Identify the preparation type.
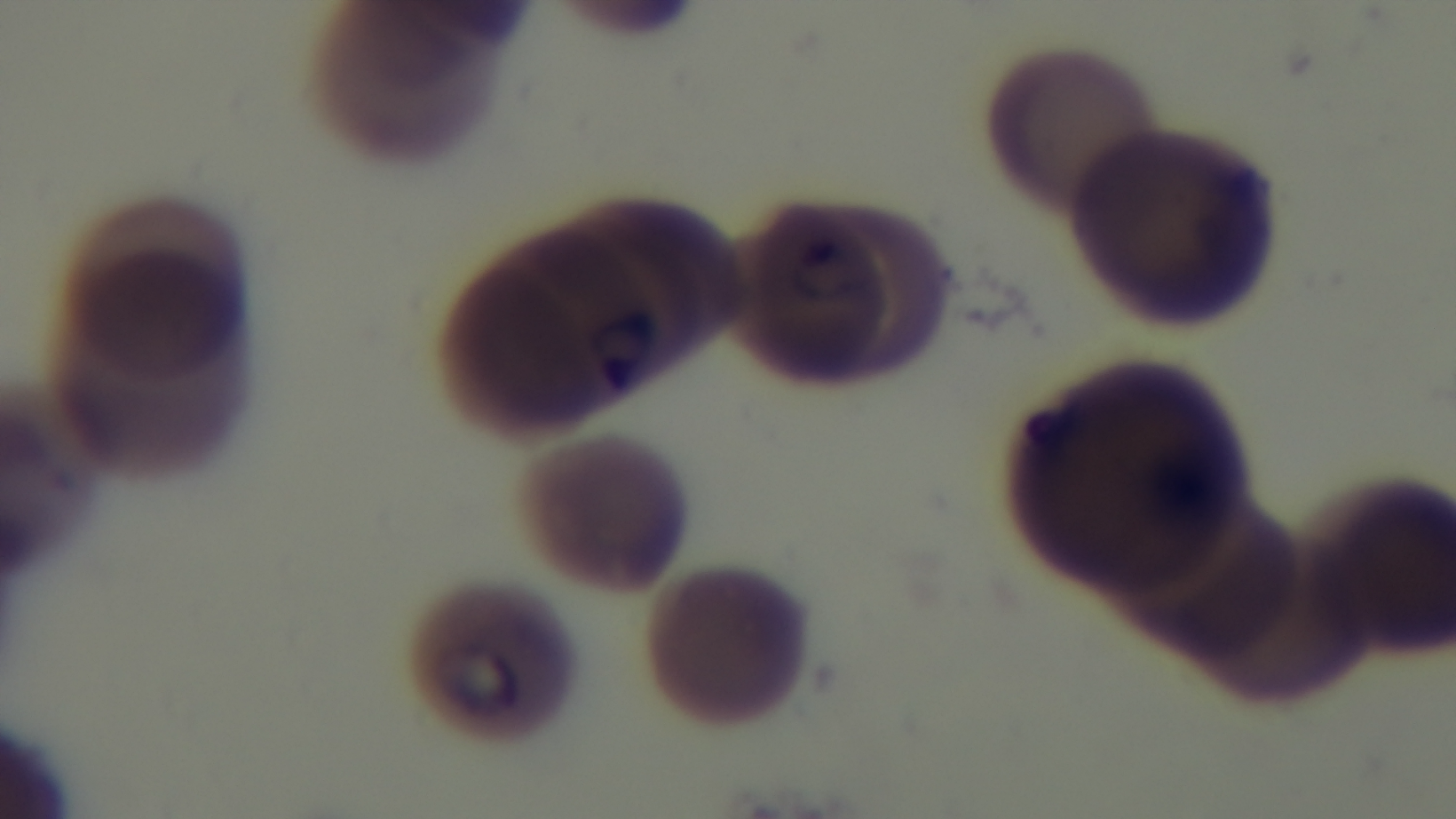
Thin.

{
  "stain": "Giemsa",
  "field_of_view": "single",
  "objective": "100x oil immersion",
  "capture": "mounted 4K digital camera",
  "malaria_status": "infected",
  "modality": "light microscopy"
}